Locate malaria parasites and leukocytes.
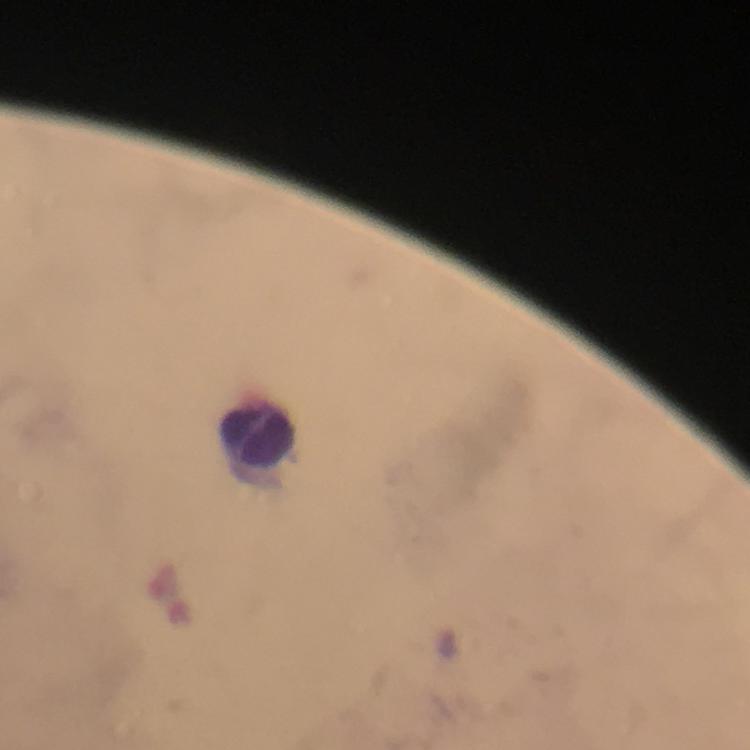

No malaria parasites seen.
Approximate object centers, in pixels from the top-left corner.
Leukocytes: (x=255, y=435).

Summary:
  - Context: from a malaria diagnostic workup
  - Cropped from: one field of view
  - Stain: Giemsa
  - Capture: smartphone mounted on the microscope
  - Magnification: 100x
  - Immersion oil: applied
  - Preparation: thick blood film
  - Image size: 750×750 pixels